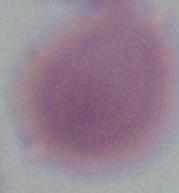
Photomicrograph. A red blood cell is shown. Captured at 1000x magnification.